Classify this cell by malaria status.
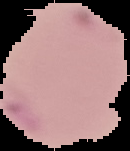
It is parasitized.

image size = 130×151 pixels
preparation = thin blood film
image type = segmented cell region on a black background